Comment on the morphology of the red blood cells.
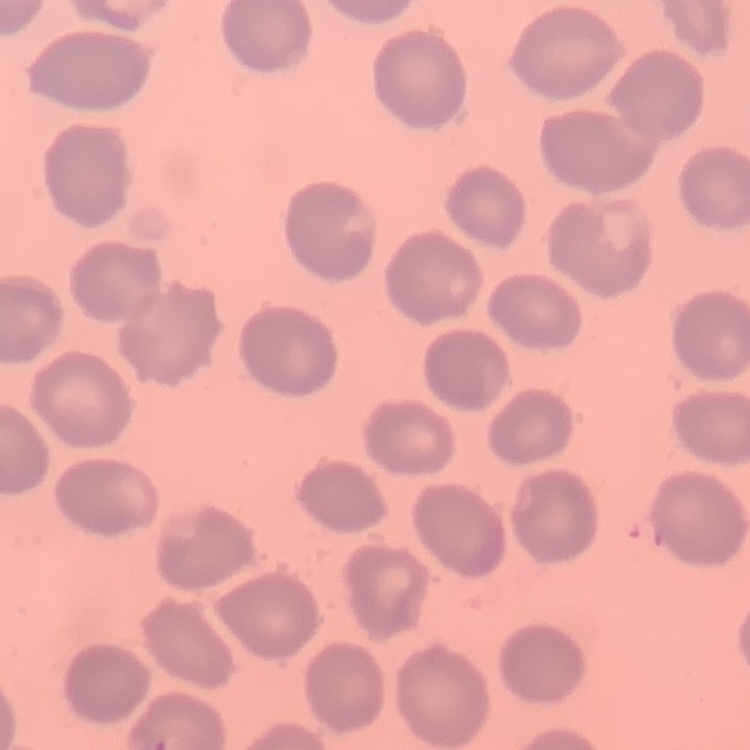
No rouleaux formation.

Summary:
  - Preparation: thin blood smear
  - Image type: square crop of a larger photomicrograph
  - Stain: Field's or Giemsa